State the blood parasite species.
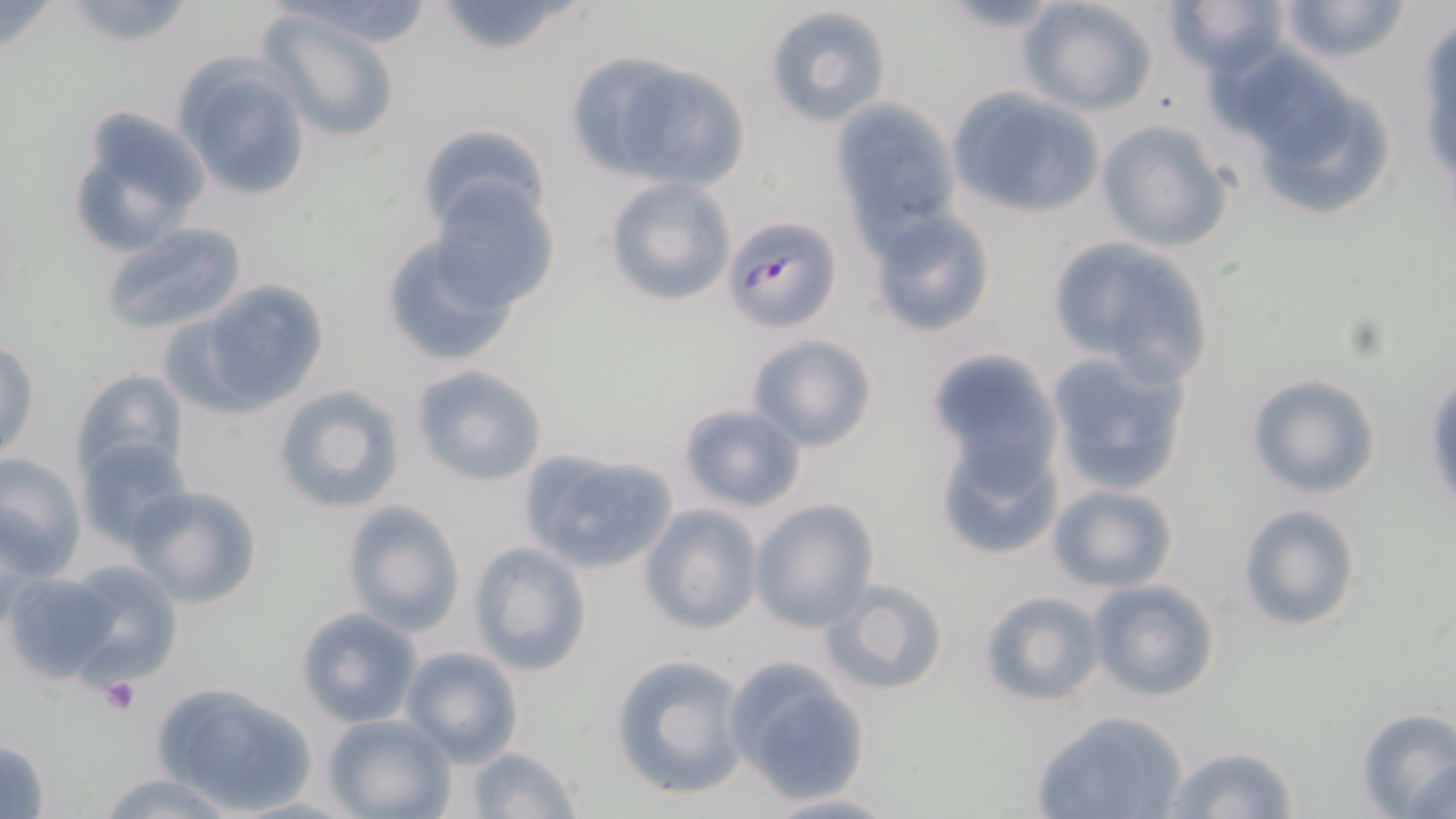

Plasmodium falciparum.

Approximate bounding boxes as [x1, y1, x2, y2] in pixels. Uninfected red blood cell locations: [60, 0, 199, 49], [266, 0, 443, 48], [1015, 0, 1162, 117], [1163, 0, 1290, 79], [1275, 0, 1412, 66], [428, 1, 593, 57], [929, 2, 1072, 34], [763, 4, 894, 128], [258, 8, 408, 146], [1411, 10, 1456, 210], [572, 52, 754, 192], [1230, 54, 1402, 223], [173, 55, 316, 204], [945, 90, 1108, 221], [831, 101, 962, 237], [64, 108, 211, 261], [1095, 118, 1236, 253], [414, 122, 552, 240], [603, 175, 736, 308], [429, 182, 561, 312], [866, 208, 997, 336], [100, 221, 248, 336], [376, 228, 528, 372], [1047, 236, 1216, 378], [185, 277, 331, 414], [744, 333, 879, 453], [0, 340, 40, 461], [1045, 348, 1194, 496], [923, 349, 1062, 474], [409, 363, 550, 487], [71, 368, 189, 483], [1245, 373, 1383, 499], [1423, 374, 1455, 517], [271, 385, 406, 514], [677, 402, 807, 513], [936, 434, 1064, 560], [75, 438, 189, 548], [515, 450, 679, 576], [0, 453, 87, 581], [1048, 483, 1178, 593], [128, 484, 266, 608], [750, 498, 879, 631], [342, 499, 467, 634], [641, 503, 762, 634], [1236, 503, 1361, 632], [469, 542, 593, 677], [58, 559, 186, 686], [3, 571, 120, 684], [1087, 578, 1219, 702], [822, 579, 950, 697], [978, 590, 1104, 707], [296, 607, 423, 727], [400, 645, 524, 766], [610, 654, 748, 800], [724, 659, 872, 804], [151, 679, 315, 814], [1355, 707, 1456, 818], [1029, 709, 1191, 819], [323, 713, 456, 819], [0, 737, 53, 817], [462, 744, 582, 819], [1162, 746, 1301, 819], [1414, 760, 1455, 817], [93, 772, 240, 818], [761, 792, 900, 818]. Plasmodium falciparum-infected red blood cell locations: [722, 215, 842, 335]. Platelet locations: [98, 676, 143, 715]. Light microscopy. Single field of view. 1000x magnification. Thin blood smear. May-Grünwald-Giemsa stain. Image is 1456×819 pixels.